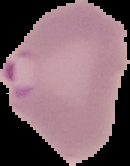

From a thin blood smear. Segmented cell region on a black background. Result: Plasmodium parasites identified. Image is 130×166 pixels.